Name the blood parasite species.
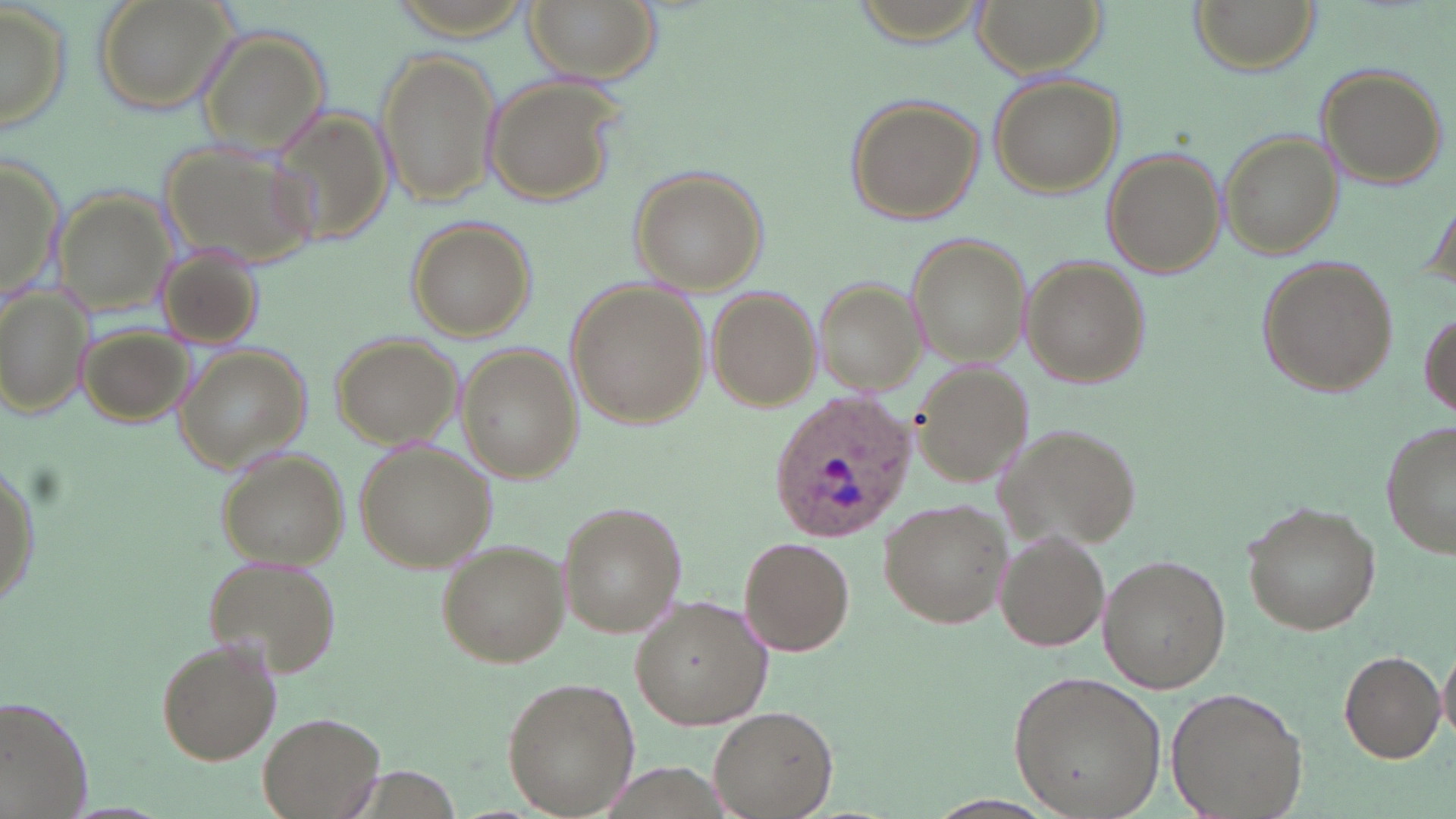
Plasmodium ovale.

image size = 1456×819 pixels
uninfected red blood cell locations = approximate bounding boxes as [x1, y1, x2, y2] in pixels: [95, 0, 236, 116], [522, 0, 658, 83], [974, 0, 1102, 77], [1191, 0, 1316, 74], [0, 4, 73, 139], [198, 26, 331, 164], [376, 48, 500, 207], [1314, 64, 1447, 188], [988, 72, 1125, 195], [485, 75, 625, 207], [847, 96, 987, 224], [268, 102, 400, 246], [1221, 132, 1344, 259], [157, 139, 319, 273], [1104, 148, 1226, 278], [1, 150, 62, 309], [631, 168, 770, 295], [53, 191, 177, 315], [408, 220, 534, 339], [906, 233, 1030, 365], [156, 243, 267, 354], [1256, 255, 1399, 398], [1022, 257, 1149, 389], [812, 274, 925, 395], [565, 277, 708, 431], [1, 281, 90, 422], [707, 285, 821, 409], [1418, 309, 1454, 421], [77, 318, 196, 427], [331, 332, 461, 448], [176, 344, 311, 469], [457, 344, 581, 480], [913, 359, 1036, 486], [1381, 420, 1456, 561], [996, 421, 1141, 550], [356, 440, 497, 571], [216, 448, 350, 568], [1, 457, 39, 615], [878, 496, 1012, 629], [557, 500, 688, 638], [1240, 500, 1382, 638], [992, 529, 1110, 653], [737, 536, 854, 657], [436, 539, 569, 667], [1098, 553, 1231, 693], [203, 555, 340, 679], [629, 595, 774, 730], [156, 637, 282, 766], [1438, 643, 1456, 747], [1338, 650, 1445, 764], [1008, 670, 1166, 818], [501, 677, 641, 813], [1166, 687, 1308, 819], [1, 695, 97, 818], [708, 705, 837, 817], [259, 710, 384, 817]
Plasmodium ovale-infected red blood cell locations = approximate bounding boxes as [x1, y1, x2, y2] in pixels: [765, 392, 918, 544]
magnification = 1000x
stain = May-Grünwald-Giemsa
field of view = single
modality = light microscopy
preparation = thin blood smear